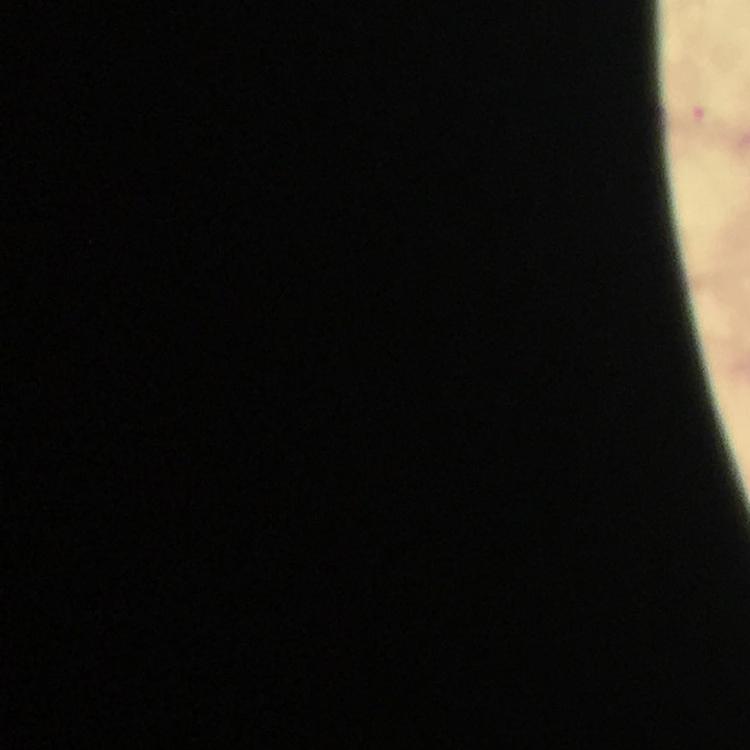
stain: Giemsa
capture: smartphone mounted on the microscope
preparation: thick blood film
immersion_oil: used
cropped_from: one field of view
plasmodium_parasite_locations: 'approximate object centers, in pixels from the top-left corner: (x=696, y=119)'
magnification: 100x
image_size: 750×750 pixels
context: from a malaria diagnostic workup